Name the parasite shown.
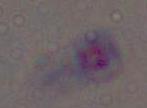

This is Toxoplasma gondii.

Photomicrograph. 1000x magnification.